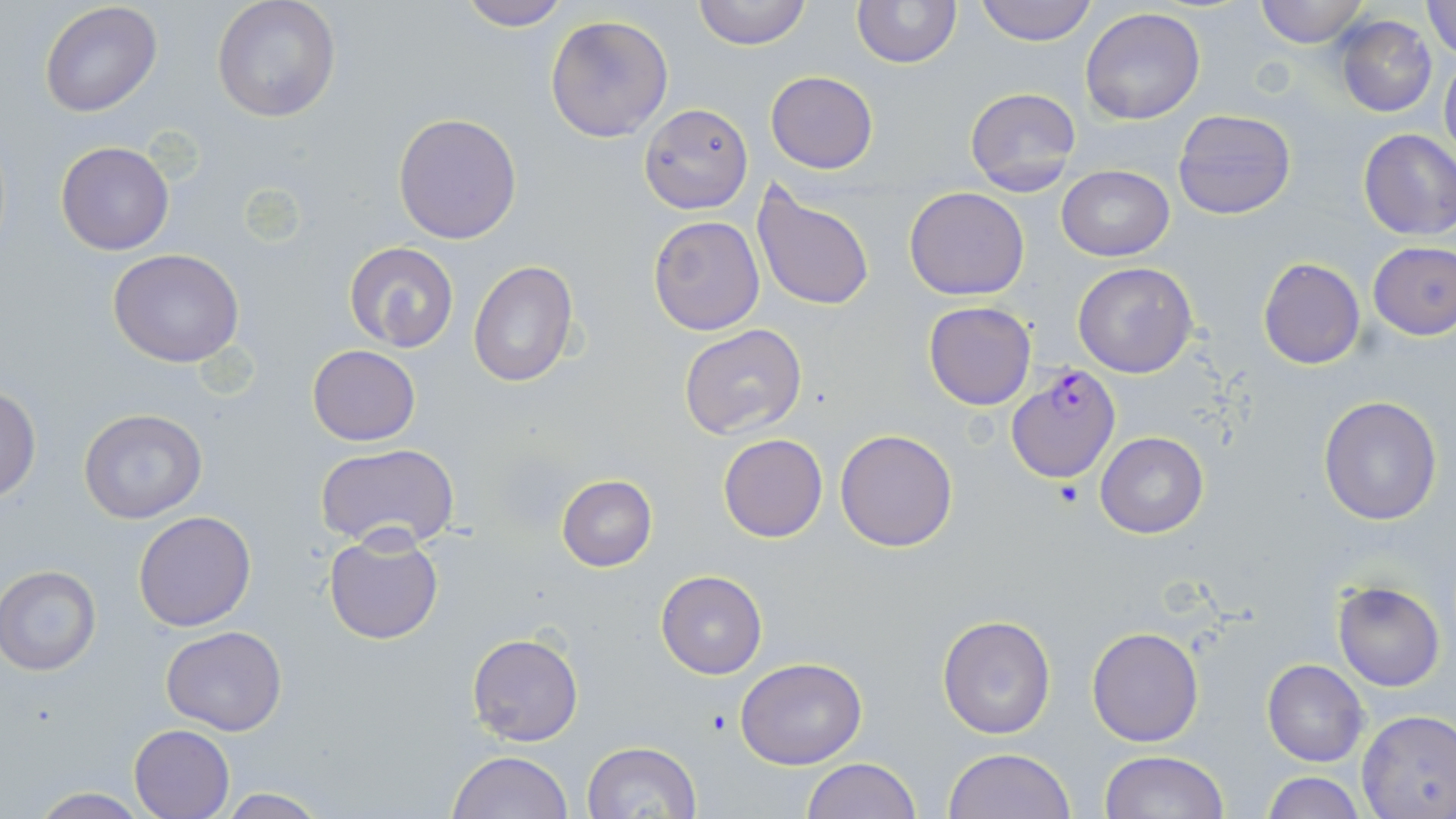
slide-level diagnosis = Plasmodium falciparum
uninfected red blood cell locations = approximate bounding boxes as (x1, y1, x2, y2) in pixels: (454, 0, 575, 30), (692, 0, 812, 50), (850, 0, 961, 69), (976, 0, 1096, 46), (1253, 0, 1369, 47), (39, 1, 162, 117), (211, 1, 342, 124), (1422, 2, 1456, 56), (1080, 8, 1207, 125), (546, 13, 674, 142), (1336, 16, 1437, 116), (1440, 48, 1456, 163), (766, 71, 877, 174), (963, 87, 1082, 194), (639, 104, 753, 213), (1172, 108, 1297, 221), (393, 112, 523, 245), (1357, 129, 1456, 240), (54, 139, 176, 256), (1057, 164, 1174, 261), (750, 182, 877, 315), (904, 186, 1030, 302), (647, 215, 764, 335), (1368, 241, 1456, 340), (344, 242, 459, 352), (109, 248, 246, 367), (1258, 258, 1365, 369), (468, 261, 578, 389), (1071, 261, 1199, 379), (923, 302, 1035, 410), (679, 324, 808, 441), (307, 345, 420, 446), (0, 386, 42, 502), (1317, 393, 1443, 526), (77, 409, 207, 523), (835, 428, 959, 551), (1095, 431, 1209, 539), (718, 433, 828, 543), (314, 442, 459, 549), (555, 474, 658, 571), (133, 511, 256, 630), (323, 533, 444, 645), (1, 566, 101, 675), (655, 570, 767, 679), (1331, 579, 1446, 692), (936, 614, 1056, 740), (160, 626, 287, 735), (1086, 626, 1205, 747), (466, 633, 583, 748), (735, 656, 867, 769), (1262, 660, 1368, 766), (1356, 709, 1456, 818), (129, 724, 235, 818), (583, 740, 702, 819), (943, 746, 1076, 819), (447, 751, 574, 819), (1099, 751, 1228, 819), (802, 757, 922, 818), (1260, 773, 1367, 818), (26, 787, 153, 818), (216, 788, 331, 818)
field of view = one of a larger specimen
image size = 1456×819 pixels
stain = May-Grünwald-Giemsa
modality = light microscopy
magnification = 1000x
preparation = thin blood film
Plasmodium falciparum-infected red blood cell locations = approximate bounding boxes as (x1, y1, x2, y2) in pixels: (1009, 364, 1123, 484)